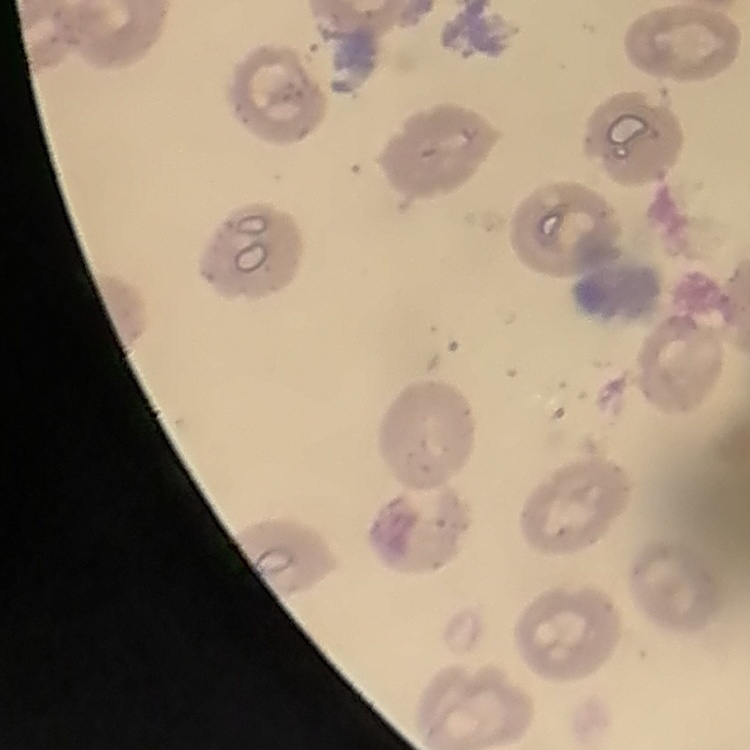 The red blood cells show no rouleaux formation. Thin peripheral smear. Square crop of a larger photomicrograph. Field's or Giemsa stain.